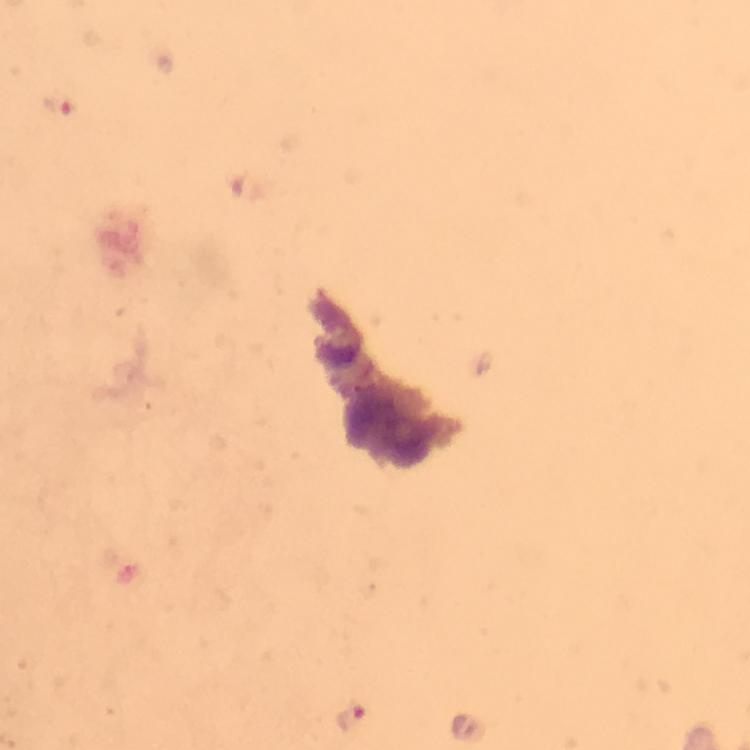

Approximate centers as (x, y) in pixels.
Summary:
  - Plasmodium parasite locations: (62, 99), (353, 718)
  - Capture: smartphone mounted on the microscope
  - Stain: Giemsa
  - Image size: 750×750 pixels
  - Immersion oil: applied
  - Context: from a malaria diagnostic workup
  - Cropped from: one field of view
  - Preparation: thick blood film
  - Magnification: 100x